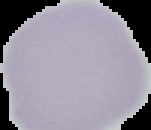

image size = 151×130 pixels
image type = segmented cell region with the area outside set to black
preparation = thin blood smear
result = no Plasmodium parasites seen